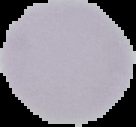

From a thin blood smear. Image is 136×127 pixels. The area outside the segmented cell region is set to black. Malaria status: uninfected.